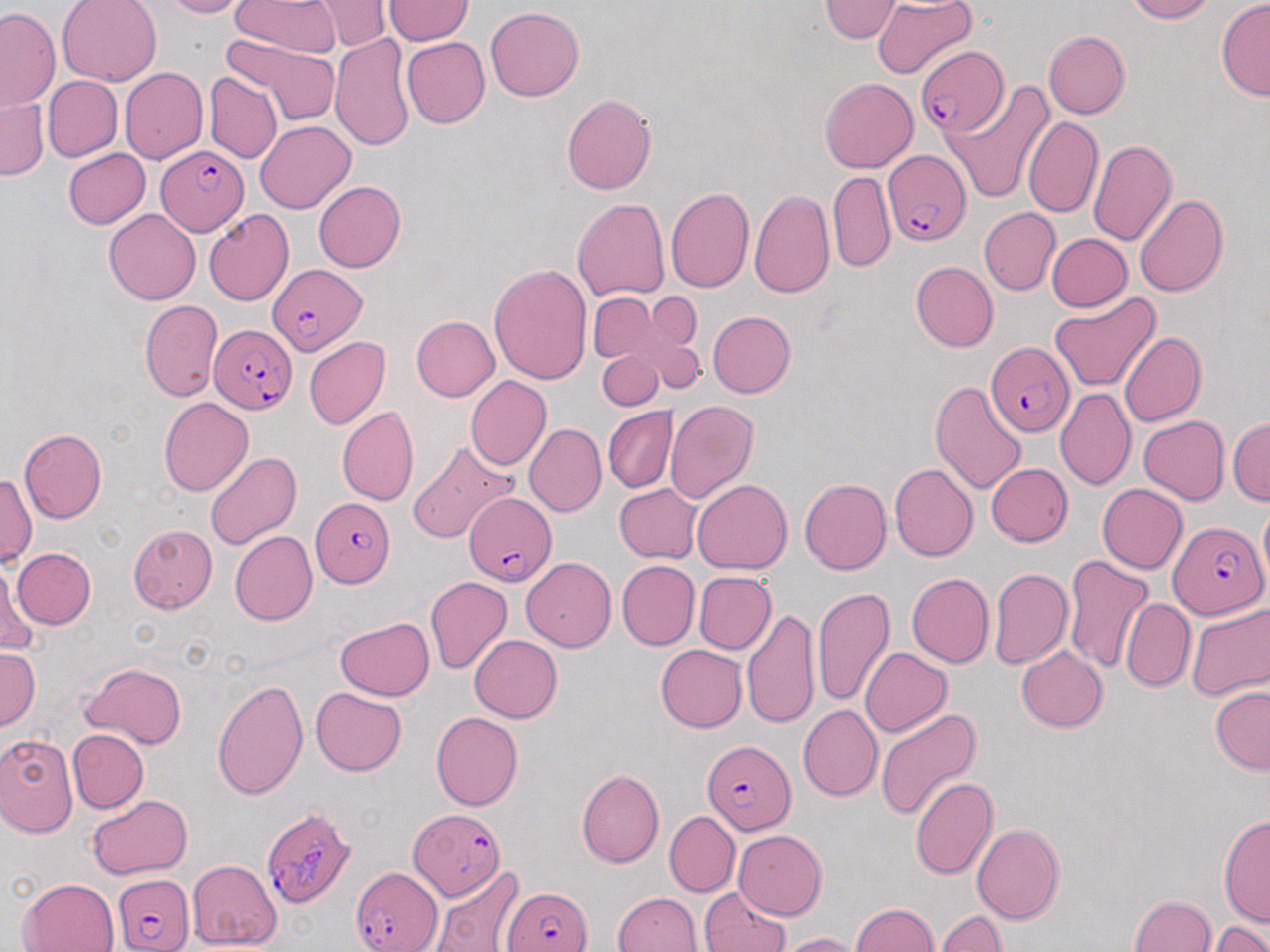

Summary:
  - Coordinate format: approximate bounding boxes as named x1/y1/x2/y2 corners in pixels
  - Uninfected red blood cell locations: (x1=55, y1=0, x2=161, y2=85), (x1=156, y1=0, x2=247, y2=17), (x1=231, y1=0, x2=338, y2=55), (x1=320, y1=0, x2=386, y2=51), (x1=384, y1=0, x2=471, y2=44), (x1=821, y1=0, x2=902, y2=43), (x1=1118, y1=0, x2=1221, y2=23), (x1=1215, y1=1, x2=1270, y2=101), (x1=872, y1=2, x2=978, y2=82), (x1=1, y1=7, x2=63, y2=114), (x1=483, y1=8, x2=584, y2=102), (x1=1042, y1=29, x2=1130, y2=120), (x1=329, y1=32, x2=417, y2=155), (x1=402, y1=37, x2=489, y2=128), (x1=218, y1=40, x2=342, y2=129), (x1=120, y1=68, x2=207, y2=164), (x1=206, y1=74, x2=281, y2=167), (x1=44, y1=75, x2=121, y2=163), (x1=820, y1=78, x2=917, y2=173), (x1=942, y1=83, x2=1053, y2=203), (x1=560, y1=93, x2=658, y2=196), (x1=0, y1=95, x2=46, y2=181), (x1=1026, y1=115, x2=1103, y2=219), (x1=257, y1=120, x2=355, y2=213), (x1=1089, y1=137, x2=1176, y2=246), (x1=60, y1=147, x2=148, y2=230), (x1=829, y1=171, x2=895, y2=271), (x1=314, y1=181, x2=406, y2=273), (x1=665, y1=186, x2=753, y2=293), (x1=750, y1=188, x2=834, y2=298), (x1=1133, y1=190, x2=1228, y2=300), (x1=573, y1=197, x2=669, y2=304), (x1=980, y1=208, x2=1059, y2=296), (x1=105, y1=209, x2=201, y2=305), (x1=203, y1=210, x2=294, y2=305), (x1=1045, y1=233, x2=1130, y2=312), (x1=488, y1=263, x2=593, y2=384), (x1=911, y1=263, x2=998, y2=353), (x1=589, y1=292, x2=659, y2=364), (x1=647, y1=292, x2=702, y2=349), (x1=1048, y1=292, x2=1161, y2=394), (x1=138, y1=296, x2=222, y2=402), (x1=708, y1=311, x2=796, y2=397), (x1=409, y1=315, x2=499, y2=401), (x1=1120, y1=331, x2=1205, y2=426), (x1=303, y1=337, x2=390, y2=430), (x1=646, y1=337, x2=704, y2=395), (x1=599, y1=352, x2=660, y2=411), (x1=466, y1=378, x2=553, y2=470), (x1=931, y1=380, x2=1026, y2=495), (x1=1056, y1=387, x2=1138, y2=490), (x1=159, y1=397, x2=254, y2=495), (x1=665, y1=400, x2=757, y2=508), (x1=336, y1=408, x2=418, y2=506), (x1=603, y1=408, x2=676, y2=493), (x1=1136, y1=415, x2=1229, y2=505), (x1=1227, y1=417, x2=1270, y2=505), (x1=523, y1=424, x2=605, y2=518), (x1=16, y1=428, x2=108, y2=524), (x1=406, y1=443, x2=516, y2=542), (x1=204, y1=448, x2=302, y2=551), (x1=984, y1=463, x2=1071, y2=547), (x1=890, y1=465, x2=978, y2=561), (x1=1, y1=469, x2=36, y2=569), (x1=800, y1=476, x2=893, y2=574), (x1=691, y1=478, x2=791, y2=573), (x1=1097, y1=482, x2=1190, y2=574), (x1=612, y1=483, x2=702, y2=563), (x1=127, y1=525, x2=214, y2=615), (x1=231, y1=532, x2=318, y2=624), (x1=12, y1=547, x2=96, y2=629), (x1=1062, y1=552, x2=1155, y2=673), (x1=521, y1=558, x2=614, y2=651), (x1=617, y1=560, x2=699, y2=649), (x1=989, y1=566, x2=1072, y2=669), (x1=1, y1=567, x2=42, y2=657), (x1=693, y1=571, x2=776, y2=656), (x1=907, y1=573, x2=995, y2=668), (x1=425, y1=576, x2=511, y2=675), (x1=813, y1=585, x2=895, y2=707), (x1=1121, y1=598, x2=1194, y2=692), (x1=1185, y1=602, x2=1270, y2=704), (x1=744, y1=607, x2=817, y2=727), (x1=333, y1=616, x2=435, y2=702), (x1=468, y1=634, x2=563, y2=723), (x1=1016, y1=644, x2=1109, y2=732), (x1=656, y1=645, x2=747, y2=733), (x1=858, y1=646, x2=950, y2=738), (x1=0, y1=648, x2=39, y2=730), (x1=78, y1=660, x2=188, y2=748), (x1=70, y1=669, x2=169, y2=814), (x1=212, y1=676, x2=309, y2=803), (x1=311, y1=685, x2=407, y2=774), (x1=1209, y1=685, x2=1269, y2=773), (x1=798, y1=705, x2=883, y2=802), (x1=873, y1=708, x2=980, y2=821), (x1=429, y1=711, x2=523, y2=810), (x1=66, y1=728, x2=147, y2=813), (x1=0, y1=732, x2=80, y2=838), (x1=579, y1=768, x2=665, y2=868), (x1=909, y1=776, x2=997, y2=880), (x1=86, y1=795, x2=192, y2=879), (x1=1218, y1=811, x2=1270, y2=924), (x1=664, y1=812, x2=738, y2=897), (x1=971, y1=823, x2=1066, y2=923), (x1=733, y1=828, x2=828, y2=918), (x1=186, y1=859, x2=280, y2=949), (x1=428, y1=866, x2=523, y2=952), (x1=17, y1=875, x2=119, y2=952), (x1=700, y1=888, x2=792, y2=952), (x1=612, y1=891, x2=702, y2=952), (x1=1128, y1=891, x2=1218, y2=952), (x1=850, y1=903, x2=943, y2=952), (x1=938, y1=909, x2=1007, y2=952), (x1=1210, y1=918, x2=1267, y2=952), (x1=779, y1=932, x2=862, y2=952)
  - Plasmodium falciparum-infected red blood cell locations: (x1=916, y1=44, x2=1006, y2=138), (x1=155, y1=143, x2=249, y2=233), (x1=884, y1=147, x2=971, y2=247), (x1=266, y1=265, x2=367, y2=356), (x1=212, y1=323, x2=297, y2=417), (x1=984, y1=339, x2=1073, y2=435), (x1=461, y1=491, x2=559, y2=588), (x1=311, y1=496, x2=395, y2=589), (x1=1166, y1=518, x2=1266, y2=621), (x1=703, y1=741, x2=794, y2=833), (x1=260, y1=806, x2=355, y2=908), (x1=408, y1=807, x2=509, y2=901), (x1=351, y1=864, x2=445, y2=952), (x1=110, y1=874, x2=193, y2=952), (x1=503, y1=883, x2=592, y2=952)
  - Slide-level diagnosis: Plasmodium falciparum
  - Magnification: 1000x
  - Preparation: thin blood film
  - Image size: 1270×952 pixels
  - Field of view: single
  - Modality: optical microscopy
  - Stain: May-Grünwald-Giemsa